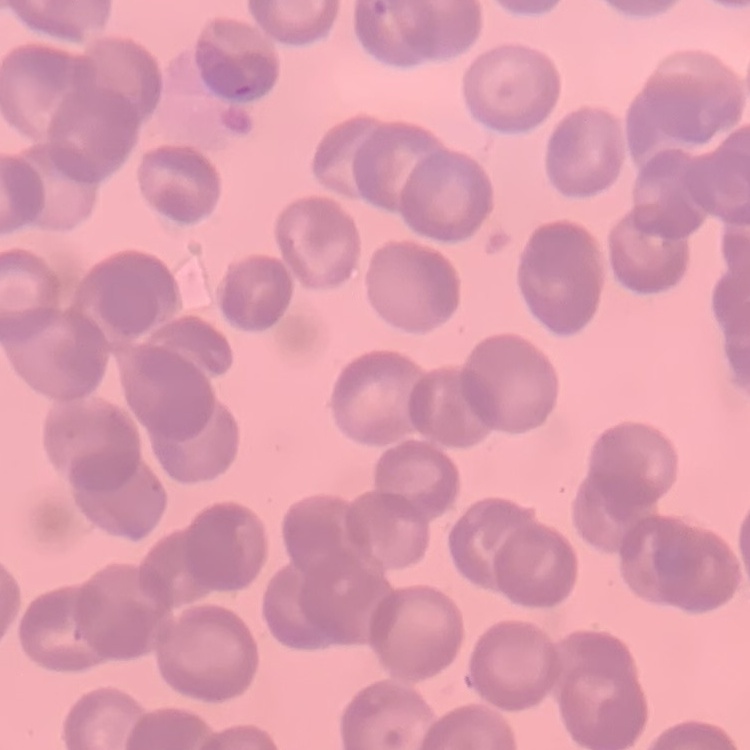

{
  "red_blood_cell_morphology": "rouleaux formation",
  "image_type": "one tile cut from a larger photomicrograph",
  "stain": "Field's or Giemsa",
  "preparation": "thin peripheral smear"
}